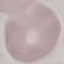

Result: no malaria parasites detected. Giemsa-stained preparation. Cell patch, automatically extracted from a larger field of view and resized to 64 × 64 pixels. Thin smear of blood. Acquired by smartphone through the microscope eyepiece.